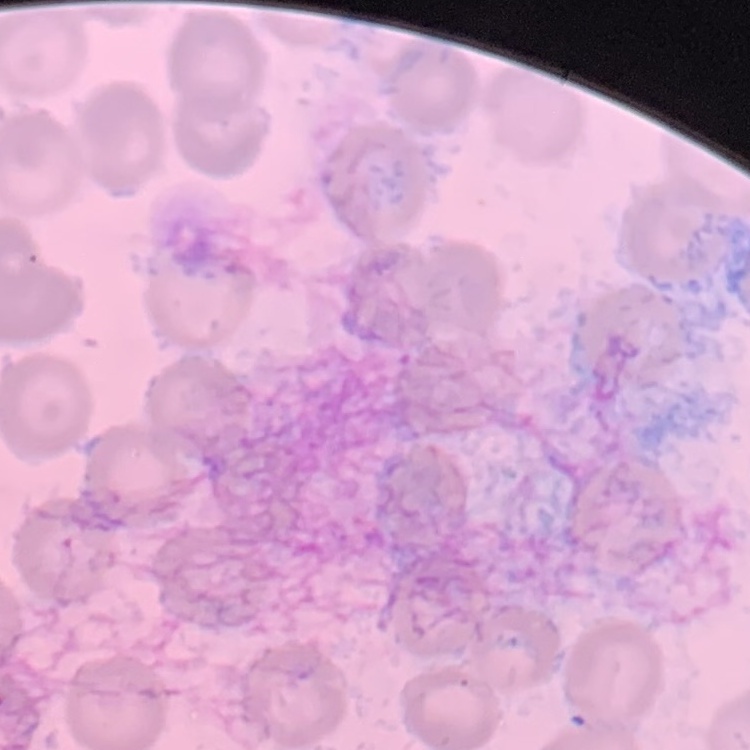

Summary:
  - Erythrocyte morphology: no rouleaux formation
  - Image type: one tile cut from a larger photomicrograph
  - Stain: Field's or Giemsa
  - Preparation: thin blood smear